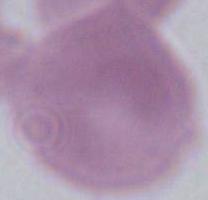
Summary:
  - Modality: micrograph
  - Identification: erythrocyte
  - Magnification: 1000x